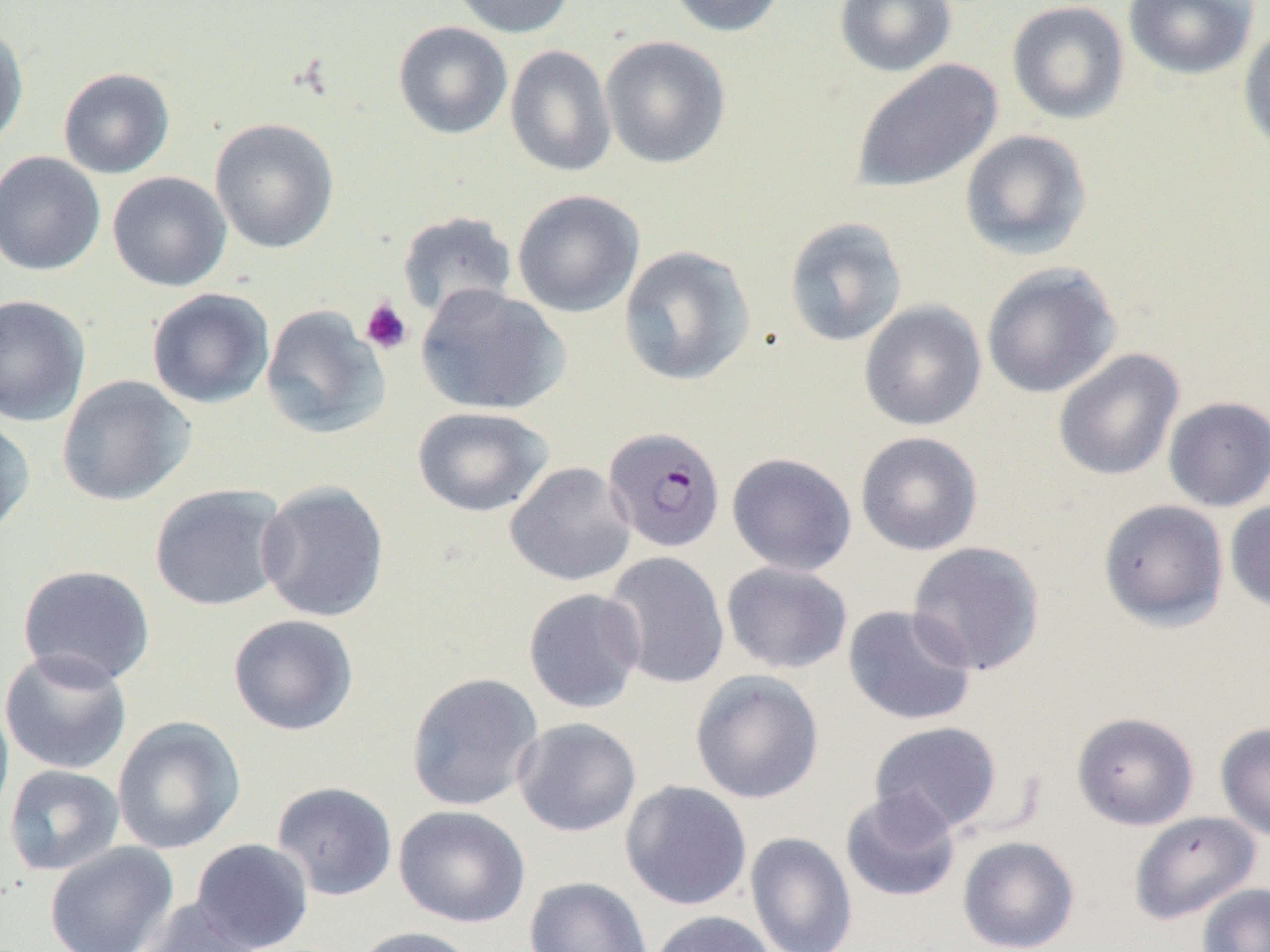

Approximate bounding boxes as named x1/y1/x2/y2 corners in pixels. Plasmodium falciparum-infected red blood cell locations: (x1=603, y1=426, x2=726, y2=553). Platelet locations: (x1=360, y1=298, x2=413, y2=355). Uninfected red blood cell locations: (x1=450, y1=0, x2=577, y2=38), (x1=667, y1=0, x2=787, y2=37), (x1=834, y1=0, x2=957, y2=77), (x1=1123, y1=0, x2=1259, y2=81), (x1=1006, y1=1, x2=1130, y2=125), (x1=1238, y1=20, x2=1270, y2=156), (x1=392, y1=21, x2=513, y2=140), (x1=0, y1=24, x2=29, y2=154), (x1=600, y1=35, x2=731, y2=168), (x1=505, y1=45, x2=617, y2=178), (x1=850, y1=59, x2=1003, y2=194), (x1=58, y1=67, x2=176, y2=179), (x1=209, y1=118, x2=340, y2=254), (x1=959, y1=129, x2=1092, y2=260), (x1=0, y1=152, x2=106, y2=276), (x1=107, y1=171, x2=232, y2=292), (x1=512, y1=189, x2=644, y2=318), (x1=397, y1=211, x2=518, y2=320), (x1=783, y1=216, x2=907, y2=347), (x1=618, y1=245, x2=756, y2=386), (x1=980, y1=262, x2=1122, y2=398), (x1=415, y1=284, x2=569, y2=415), (x1=146, y1=288, x2=275, y2=409), (x1=0, y1=294, x2=90, y2=426), (x1=859, y1=300, x2=987, y2=431), (x1=260, y1=305, x2=390, y2=440), (x1=1053, y1=348, x2=1184, y2=482), (x1=56, y1=374, x2=197, y2=507), (x1=1163, y1=396, x2=1270, y2=512), (x1=412, y1=406, x2=553, y2=517), (x1=0, y1=413, x2=35, y2=542), (x1=855, y1=432, x2=983, y2=556), (x1=727, y1=452, x2=857, y2=576), (x1=505, y1=462, x2=636, y2=587), (x1=257, y1=479, x2=390, y2=623), (x1=149, y1=483, x2=289, y2=611), (x1=1098, y1=499, x2=1229, y2=631), (x1=1225, y1=500, x2=1270, y2=614), (x1=907, y1=541, x2=1045, y2=675), (x1=602, y1=552, x2=730, y2=690), (x1=721, y1=562, x2=853, y2=675), (x1=17, y1=564, x2=155, y2=688), (x1=523, y1=588, x2=646, y2=713), (x1=843, y1=604, x2=977, y2=726), (x1=228, y1=614, x2=359, y2=736), (x1=0, y1=649, x2=133, y2=775), (x1=690, y1=670, x2=824, y2=804), (x1=406, y1=672, x2=544, y2=812), (x1=0, y1=693, x2=14, y2=828), (x1=1072, y1=712, x2=1199, y2=830), (x1=112, y1=716, x2=246, y2=854), (x1=512, y1=717, x2=642, y2=838), (x1=869, y1=721, x2=1003, y2=836), (x1=1215, y1=722, x2=1270, y2=841), (x1=3, y1=764, x2=125, y2=876), (x1=620, y1=780, x2=752, y2=911), (x1=271, y1=781, x2=398, y2=901), (x1=841, y1=790, x2=961, y2=903), (x1=394, y1=805, x2=531, y2=928), (x1=1129, y1=811, x2=1262, y2=925), (x1=745, y1=831, x2=857, y2=952), (x1=957, y1=836, x2=1080, y2=952), (x1=190, y1=838, x2=314, y2=952), (x1=44, y1=841, x2=179, y2=952), (x1=524, y1=876, x2=654, y2=952), (x1=1197, y1=883, x2=1270, y2=952), (x1=139, y1=898, x2=263, y2=952), (x1=647, y1=910, x2=776, y2=952), (x1=352, y1=926, x2=481, y2=952). Slide-level diagnosis: Plasmodium falciparum. Captured at 1000x magnification. One field of a larger specimen. Image is 1270×952 pixels. Optical microscopy. Thin blood film.